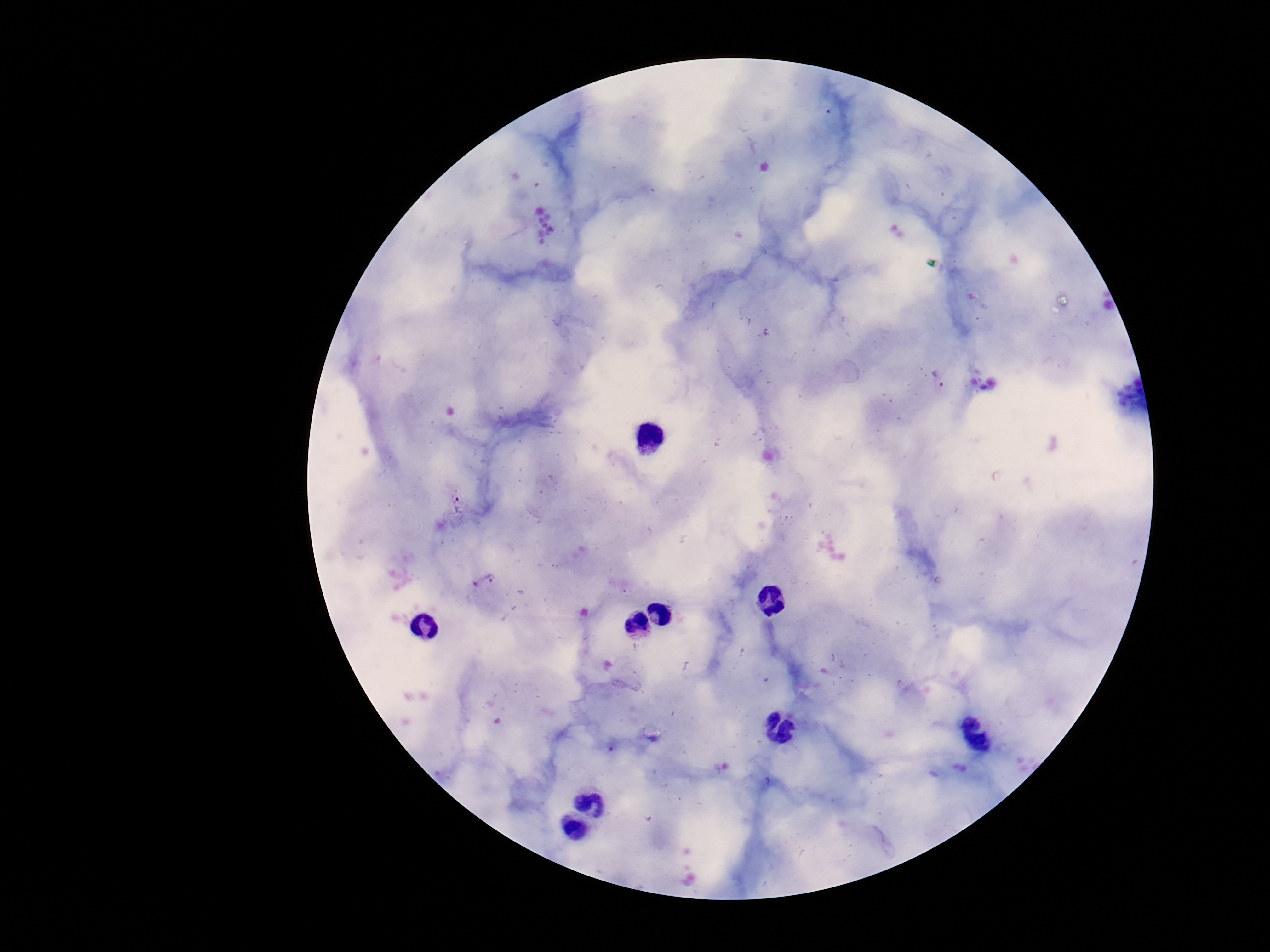
preparation = thick peripheral-blood smear
capture = smartphone camera through the microscope eyepiece
patient malaria status = infected
field of view = one from this slide
image size = 1270×952 pixels
stain = Giemsa
magnification = 100x
Plasmodium parasite locations = approximate object centers, in pixels from the top-left corner: (x=937, y=379), (x=458, y=502)